Locate every blood parasite and identify its species.
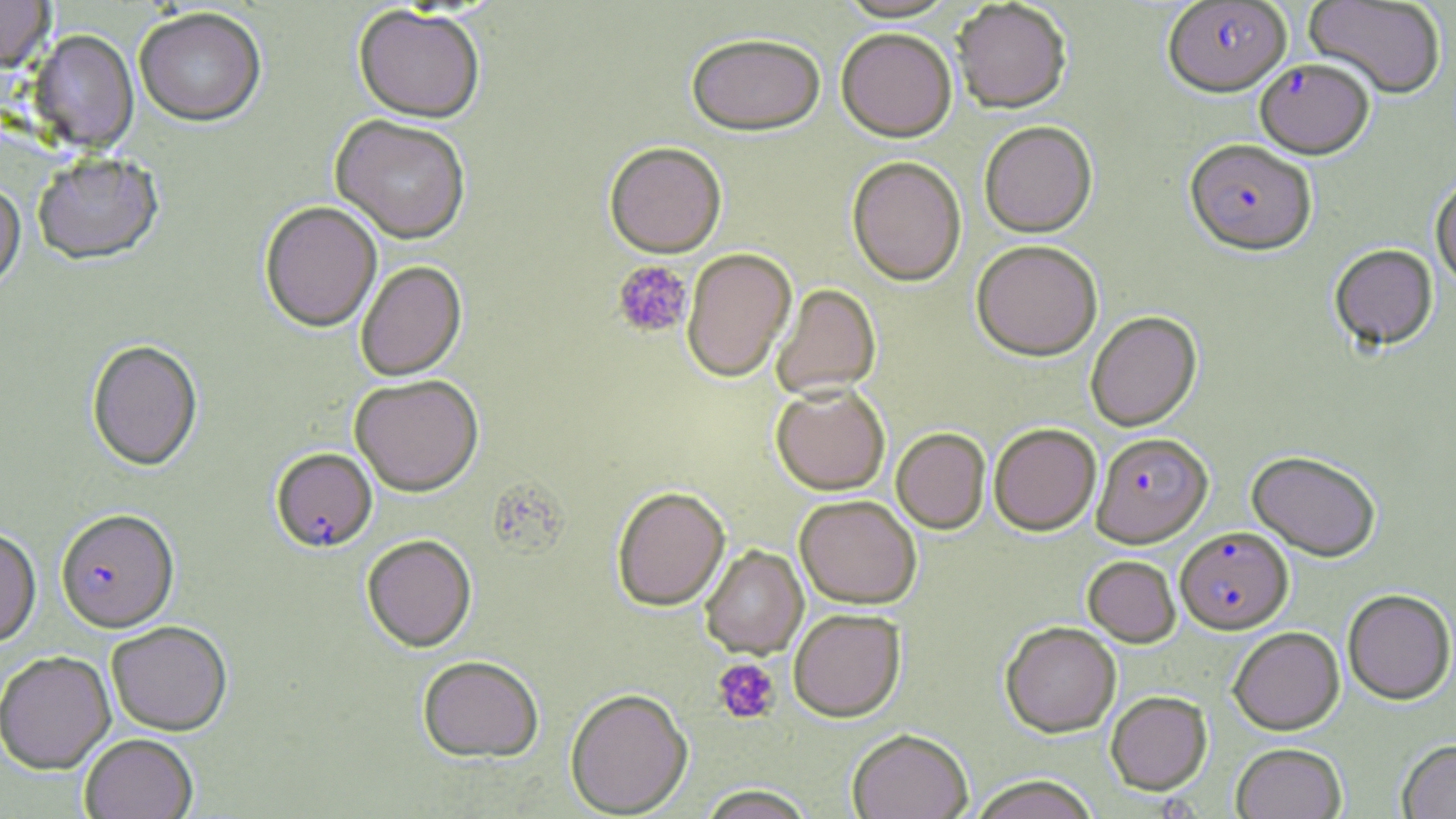

Approximate bounding boxes as [x1, y1, x2, y2] in pixels.
Plasmodium falciparum-infected red blood cells: [1161, 1, 1291, 97], [1255, 59, 1374, 159], [1185, 140, 1317, 255], [1091, 431, 1212, 547], [271, 448, 378, 554], [55, 510, 179, 634], [1175, 526, 1292, 634].
No Plasmodium ovale, Plasmodium malariae, Plasmodium vivax, Babesia divergens, or Trypanosoma brucei observed.

Platelet locations: [612, 259, 692, 339], [712, 658, 781, 725]. Uninfected red blood cell locations: [0, 0, 55, 77], [836, 0, 958, 23], [1304, 0, 1446, 99], [952, 1, 1072, 113], [352, 7, 485, 125], [134, 11, 266, 129], [836, 28, 957, 141], [28, 32, 139, 155], [686, 34, 826, 137], [330, 116, 471, 246], [979, 120, 1097, 237], [604, 143, 727, 258], [33, 155, 164, 267], [846, 156, 966, 286], [1430, 177, 1456, 287], [0, 186, 26, 295], [259, 202, 382, 334], [971, 239, 1102, 360], [1329, 244, 1438, 350], [682, 248, 796, 382], [355, 261, 467, 381], [771, 283, 881, 400], [1085, 311, 1201, 431], [87, 341, 203, 472], [350, 375, 484, 497], [771, 383, 890, 495], [989, 422, 1101, 535], [891, 428, 990, 534], [1247, 450, 1381, 561], [611, 486, 730, 611], [795, 495, 921, 608], [0, 529, 41, 647], [361, 535, 477, 653], [700, 545, 808, 659], [1083, 555, 1181, 647], [1342, 589, 1456, 704], [788, 609, 905, 722], [1000, 621, 1121, 737], [106, 622, 233, 736], [1228, 626, 1344, 734], [0, 651, 116, 776], [417, 655, 544, 763], [565, 688, 693, 817], [1106, 690, 1212, 794], [848, 728, 972, 818], [80, 734, 197, 819], [1397, 740, 1456, 818], [1231, 743, 1347, 819], [967, 775, 1100, 818], [695, 786, 817, 819]. Slide-level diagnosis: Plasmodium falciparum. One field of a larger specimen. Light microscopy. Image is 1456×819 pixels. Captured at 1000x magnification. May-Grünwald-Giemsa-stained preparation. Thin blood smear.